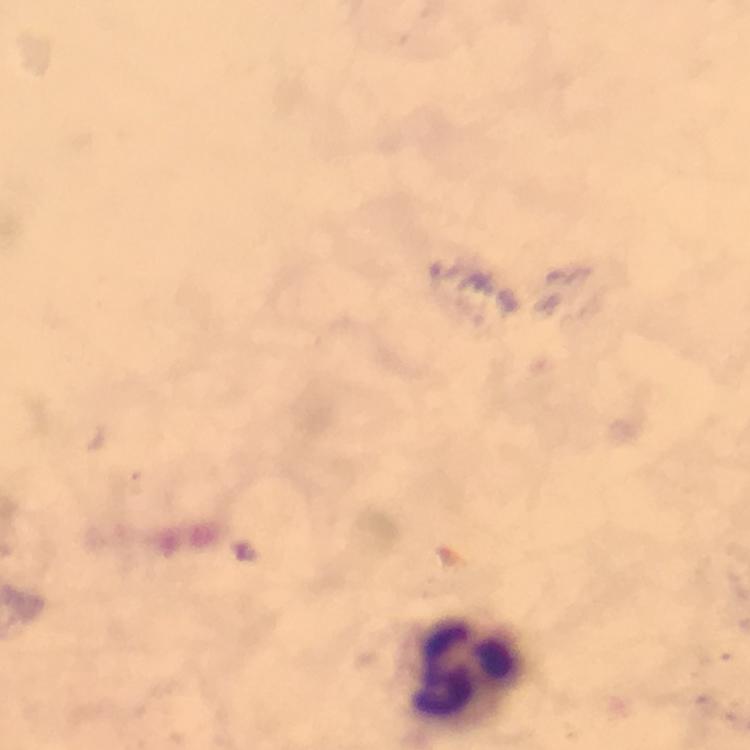
Approximate object centers, in pixels from the top-left corner. Leukocyte locations: (x=467, y=667). Giemsa stain. Cropped region of a single field of view. Thick blood smear. Photographed with a smartphone mounted on the microscope. From a malaria diagnostic workup. Immersion oil was used. 100x magnification. Malaria parasites: none seen. Image is 750×750 pixels.